State the blood parasite species.
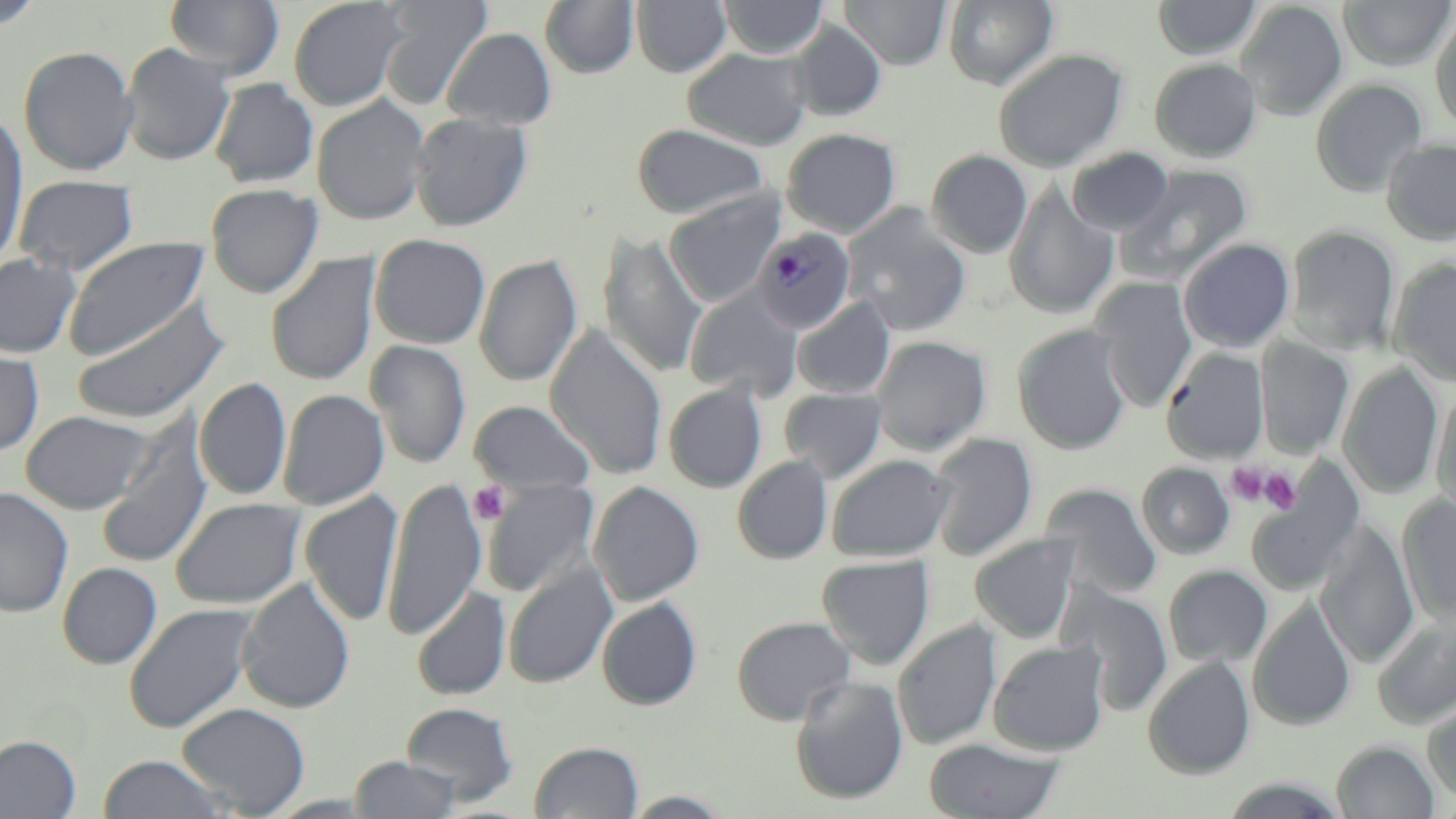

Plasmodium malariae.

Approximate bounding boxes as [x1, y1, x2, y2] in pixels. Plasmodium malariae-infected red blood cell locations: [753, 227, 856, 334]. Platelet locations: [1226, 463, 1271, 506], [1260, 469, 1302, 514], [469, 481, 511, 525]. Uninfected red blood cell locations: [164, 0, 284, 80], [288, 0, 407, 111], [380, 0, 492, 109], [632, 0, 731, 77], [719, 0, 828, 59], [840, 0, 952, 69], [944, 0, 1058, 90], [1152, 0, 1262, 61], [1235, 0, 1348, 120], [1338, 0, 1454, 70], [1, 1, 44, 29], [540, 1, 639, 78], [1430, 10, 1456, 132], [788, 20, 886, 121], [442, 27, 557, 130], [120, 42, 235, 166], [18, 45, 139, 177], [684, 48, 810, 150], [993, 48, 1129, 172], [1149, 58, 1263, 162], [209, 77, 319, 188], [1310, 78, 1428, 197], [312, 95, 430, 225], [0, 112, 30, 268], [410, 112, 532, 231], [632, 123, 770, 220], [782, 128, 901, 237], [1381, 138, 1456, 246], [1067, 147, 1174, 236], [927, 150, 1033, 258], [1118, 165, 1253, 285], [13, 175, 139, 276], [205, 183, 324, 299], [1004, 183, 1119, 320], [664, 193, 783, 307], [842, 204, 973, 336], [1285, 224, 1401, 354], [599, 231, 708, 379], [370, 233, 491, 349], [61, 237, 209, 363], [1178, 238, 1295, 352], [266, 252, 381, 386], [0, 254, 81, 359], [474, 255, 583, 387], [1390, 258, 1456, 386], [1091, 277, 1197, 412], [685, 287, 804, 401], [69, 297, 230, 426], [792, 297, 894, 398], [1012, 323, 1132, 455], [545, 326, 668, 480], [871, 335, 992, 455], [1255, 339, 1354, 458], [365, 340, 471, 469], [0, 346, 44, 456], [1163, 348, 1270, 464], [1338, 363, 1443, 500], [195, 377, 293, 501], [664, 383, 767, 493], [1431, 383, 1456, 521], [779, 387, 887, 482], [277, 389, 390, 509], [470, 399, 596, 497], [20, 410, 154, 514], [96, 416, 213, 568], [928, 433, 1037, 562], [826, 454, 953, 562], [733, 456, 833, 564], [1137, 462, 1235, 559], [1246, 477, 1363, 596], [382, 478, 487, 640], [481, 478, 599, 597], [589, 481, 704, 606], [1042, 484, 1162, 599], [0, 487, 74, 618], [299, 490, 404, 626], [1397, 496, 1456, 627], [170, 497, 307, 610], [1316, 520, 1420, 668], [970, 534, 1081, 643], [818, 554, 934, 669], [58, 562, 162, 668], [503, 562, 617, 689], [1163, 565, 1272, 668], [238, 579, 355, 714], [412, 586, 511, 701], [1063, 586, 1174, 715], [1248, 596, 1357, 731], [597, 597, 702, 710], [123, 603, 258, 734], [731, 615, 857, 726], [1372, 617, 1455, 729], [893, 620, 1001, 750], [989, 640, 1108, 756], [1143, 656, 1256, 780], [791, 675, 910, 805], [1422, 697, 1456, 805], [177, 702, 311, 816], [401, 702, 518, 803], [0, 735, 81, 818], [924, 737, 1065, 819], [530, 740, 644, 818], [1332, 740, 1440, 819], [97, 754, 230, 818], [348, 756, 462, 818], [622, 790, 736, 817]. May-Grünwald-Giemsa-stained preparation. Optical microscopy. Thin blood smear. One field of a larger specimen. Image is 1456×819 pixels. 1000x magnification.